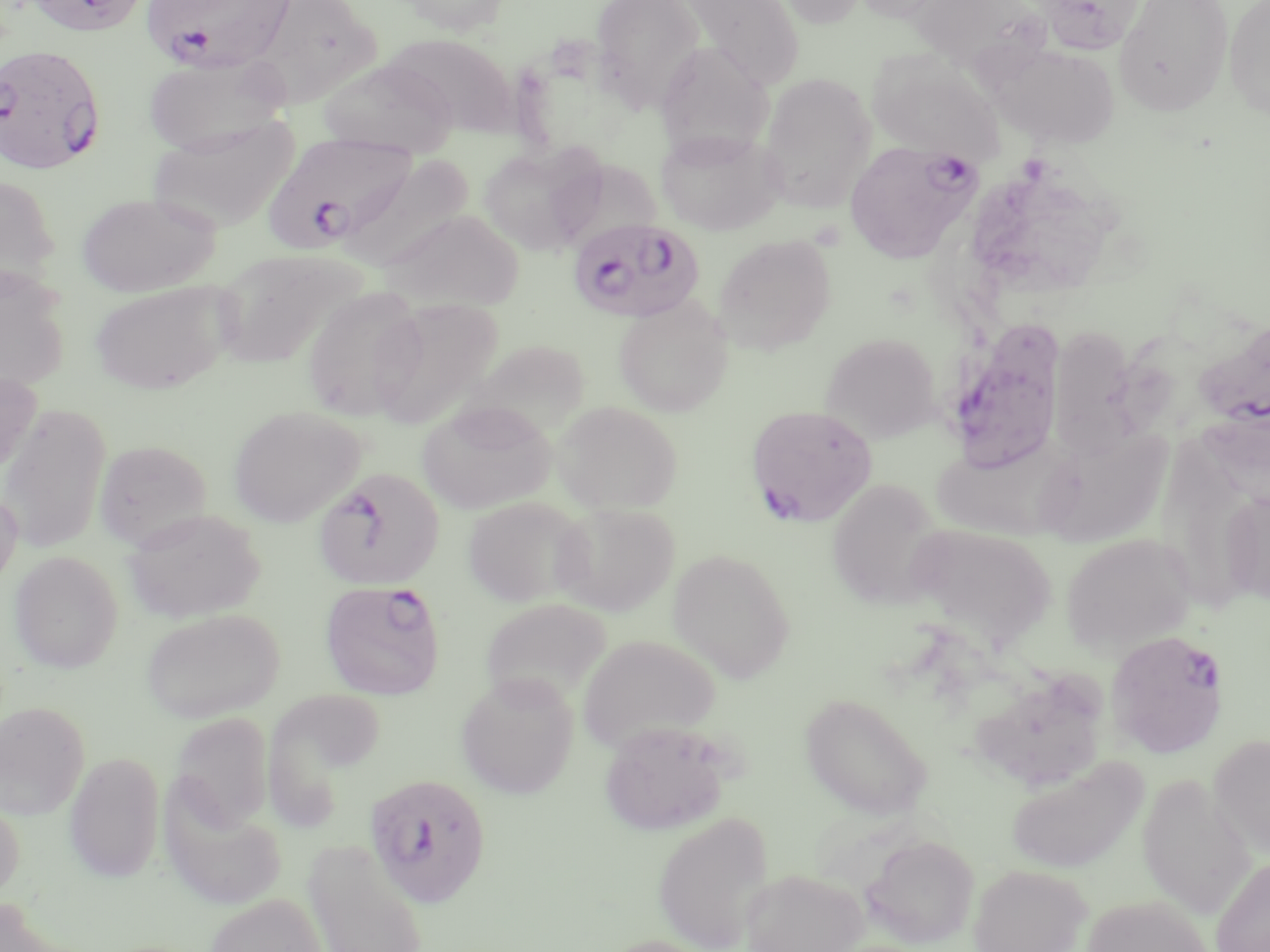
slide_level_diagnosis: Plasmodium falciparum
magnification: 1000x
modality: optical microscopy
stain: May-Grünwald-Giemsa
preparation: thin blood smear
uninfected_red_blood_cell_locations: 'approximate bounding boxes as (x1, y1, x2, y2) in pixels: (397, 0, 510, 35), (590, 0, 706, 111), (676, 0, 804, 89), (770, 0, 867, 28), (850, 0, 953, 23), (910, 0, 1042, 70), (1034, 0, 1145, 54), (1114, 0, 1234, 117), (1223, 0, 1270, 119), (248, 1, 383, 109), (382, 32, 517, 137), (655, 37, 778, 153), (993, 44, 1120, 148), (868, 52, 1003, 164), (142, 53, 290, 156), (319, 58, 460, 158), (757, 72, 876, 213), (146, 116, 299, 233), (655, 127, 784, 236), (479, 143, 604, 256), (552, 158, 667, 244), (981, 160, 1125, 285), (0, 173, 61, 293), (76, 191, 220, 297), (382, 208, 526, 311), (713, 233, 837, 355), (211, 246, 368, 368), (1, 270, 69, 392), (89, 279, 238, 395), (301, 285, 426, 420), (614, 295, 732, 417), (368, 297, 503, 428), (1053, 326, 1185, 462), (820, 331, 941, 443), (467, 338, 590, 439), (0, 367, 41, 479), (417, 400, 556, 514), (552, 401, 682, 513), (1, 403, 110, 554), (228, 405, 366, 527), (1200, 405, 1269, 509), (930, 437, 1068, 540), (1033, 438, 1194, 540), (93, 439, 213, 550), (1157, 439, 1265, 620), (0, 484, 22, 594), (1219, 490, 1270, 605), (462, 496, 590, 607), (552, 501, 680, 615), (123, 507, 264, 623), (904, 525, 1058, 652), (1062, 532, 1196, 655), (668, 548, 796, 682), (9, 550, 123, 673), (479, 598, 614, 718), (141, 607, 285, 723), (579, 635, 721, 752), (456, 673, 579, 799), (263, 689, 387, 823), (800, 692, 933, 819), (0, 701, 89, 820), (170, 712, 274, 833), (600, 720, 731, 835), (1209, 733, 1270, 859), (64, 751, 165, 883), (1005, 755, 1148, 875), (1137, 774, 1254, 920), (160, 790, 288, 910), (0, 796, 24, 900), (652, 811, 775, 952), (863, 834, 979, 948), (302, 838, 429, 952), (1211, 853, 1270, 952), (968, 863, 1092, 952), (741, 868, 868, 952), (204, 893, 328, 952), (1080, 895, 1213, 952), (0, 896, 78, 952)'
field_of_view: single
image_size: 1270×952 pixels
plasmodium_falciparum_infected_red_blood_cell_locations: 'approximate bounding boxes as (x1, y1, x2, y2) in pixels: (140, 0, 295, 73), (0, 43, 107, 175), (268, 133, 412, 252), (844, 140, 977, 263), (568, 217, 704, 322), (956, 316, 1071, 476), (1194, 319, 1270, 433), (746, 404, 878, 527), (313, 467, 444, 590), (319, 579, 447, 700), (1106, 628, 1229, 759), (364, 772, 492, 908)'